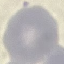

result: no malaria parasites seen
stain: Giemsa
preparation: thin smear
image_type: cell patch, automatically extracted from a larger field of view and resized to 64 × 64 pixels
capture: smartphone through the microscope eyepiece